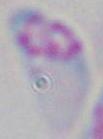
Summary:
  - Modality: micrograph
  - Identification: Toxoplasma gondii
  - Magnification: 1000x